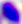

Micrograph. 400x magnification. Toxoplasma gondii is seen.